Name the parasite shown.
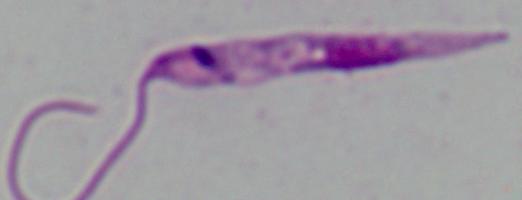
Leishmania.

Micrograph. Captured at 1000x magnification.